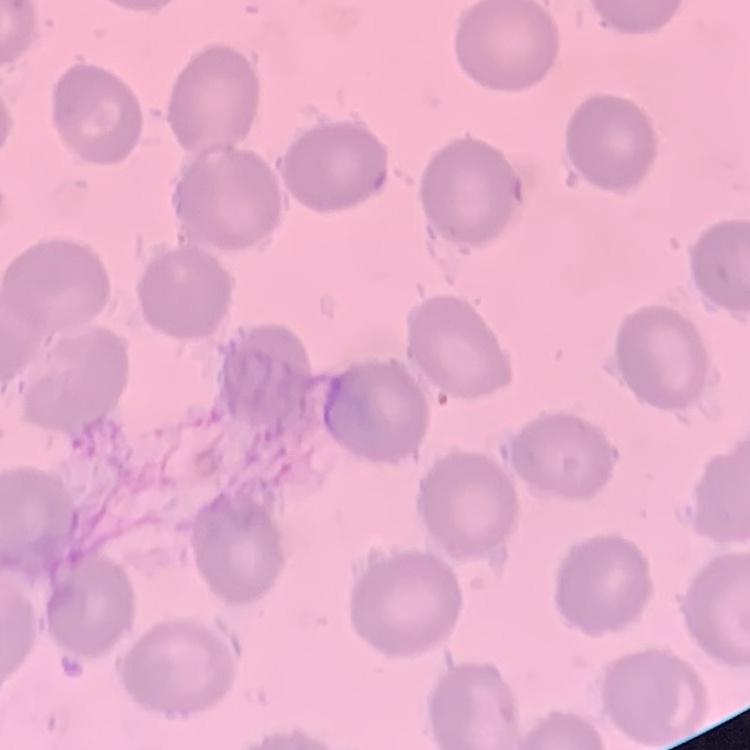
The red blood cells show no rouleaux formation. Thin blood smear. Stained with either Field's or Giemsa. One tile cut from a larger photomicrograph.